Name the parasite shown.
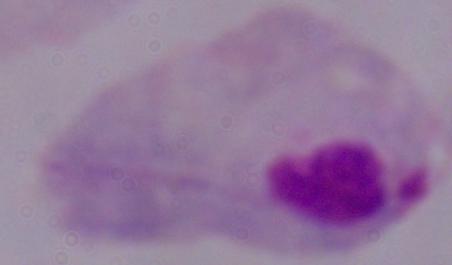
This is a trichomonad.

Captured at 1000x magnification. Micrograph.